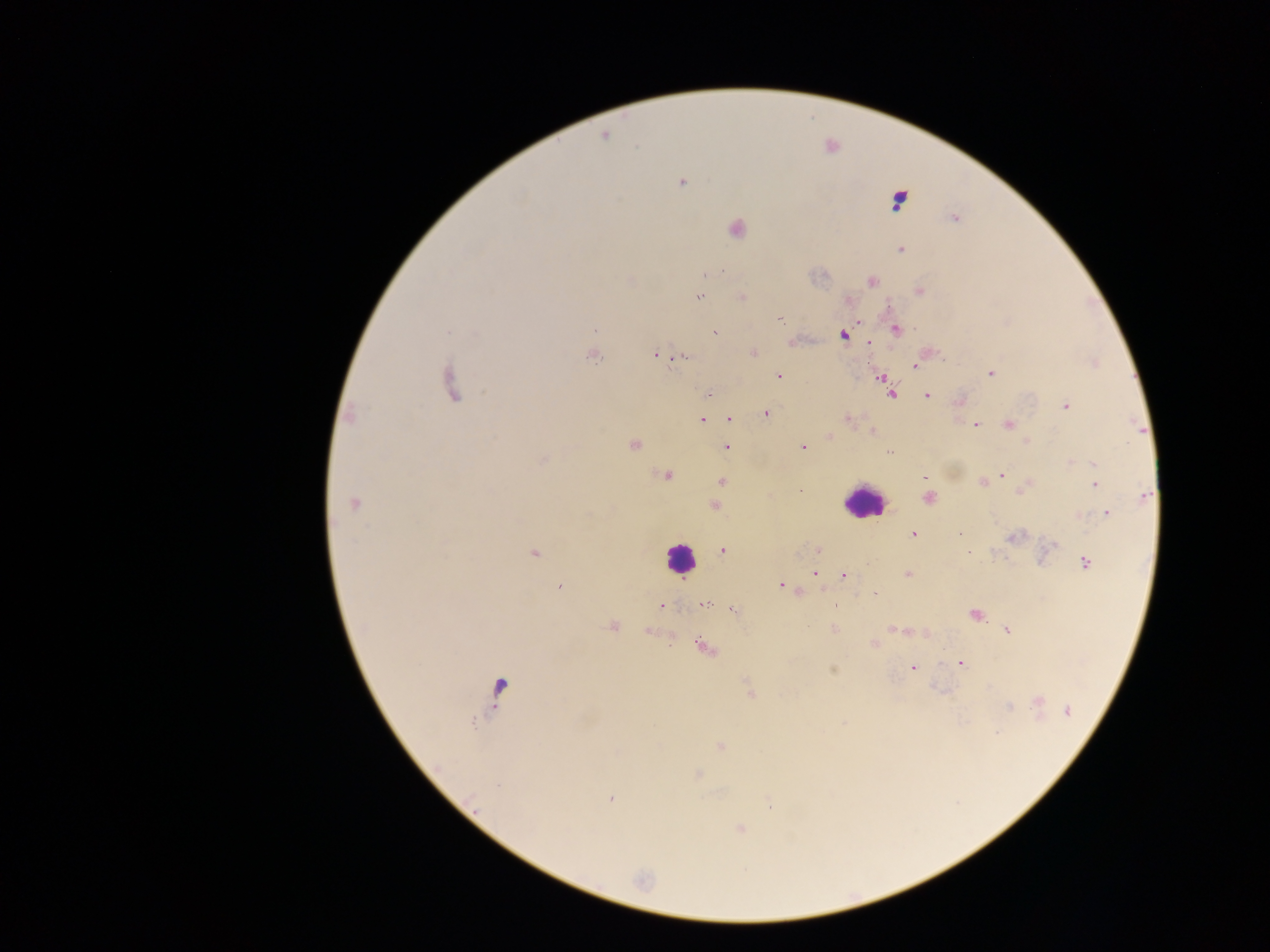

Approximate centers as {x, y} in pixels.
Summary:
  - Plasmodium parasite locations: {604, 136}, {681, 182}, {898, 200}, {954, 218}, {736, 229}, {900, 249}, {721, 271}, {709, 273}, {871, 281}, {920, 292}, {699, 296}, {742, 297}, {781, 320}, {596, 329}, {897, 329}, {447, 331}, {715, 333}, {843, 336}, {868, 343}, {753, 353}, {655, 354}, {593, 356}, {684, 357}, {1096, 363}, {914, 366}, {991, 373}, {779, 375}, {881, 378}, {451, 384}, {888, 389}, {708, 395}, {891, 395}, {927, 396}, {1066, 406}, {766, 413}, {349, 415}, {729, 419}, {847, 419}, {702, 420}, {975, 425}, {1008, 425}, {873, 431}, {829, 436}, {634, 445}, {727, 447}, {803, 447}, {888, 452}, {542, 460}, {1071, 462}, {1093, 464}, {1002, 475}, {665, 476}, {924, 477}, {721, 481}, {983, 483}, {1095, 484}, {1023, 490}, {1144, 496}, {929, 498}, {353, 503}, {714, 506}, {1108, 514}, {913, 533}, {960, 534}, {1014, 537}, {818, 549}, {1050, 549}, {723, 550}, {967, 552}, {535, 553}, {1085, 563}, {815, 573}, {908, 574}, {844, 575}, {780, 585}, {559, 587}, {875, 594}, {704, 604}, {834, 604}, {662, 606}, {733, 610}, {975, 614}, {613, 626}, {892, 628}, {833, 629}, {1007, 630}, {874, 644}, {706, 648}, {961, 664}, {912, 667}, {833, 670}, {749, 690}, {1039, 701}, {1008, 706}, {1067, 711}, {843, 722}, {720, 746}, {698, 774}, {611, 799}, {770, 804}, {740, 829}, {643, 880}
  - Leukocyte locations: {861, 502}, {679, 557}
  - Country: Ghana
  - Capture: mobile-phone photograph through a microscope
  - Image size: 1270×952 pixels
  - Field of view: single
  - Preparation: thick blood film